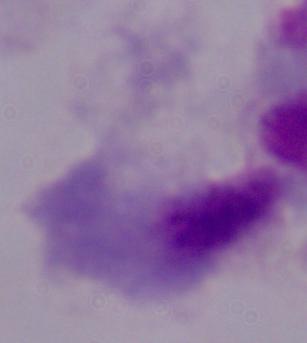
magnification = 1000x
modality = photomicrograph
identification = trichomonad